Assess this cell for malaria.
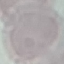

It is uninfected.

Summary:
  - Preparation: thin smear
  - Capture: smartphone camera at the microscope eyepiece
  - Image type: automatically extracted cell patch, resized to 64 × 64 pixels
  - Stain: Giemsa